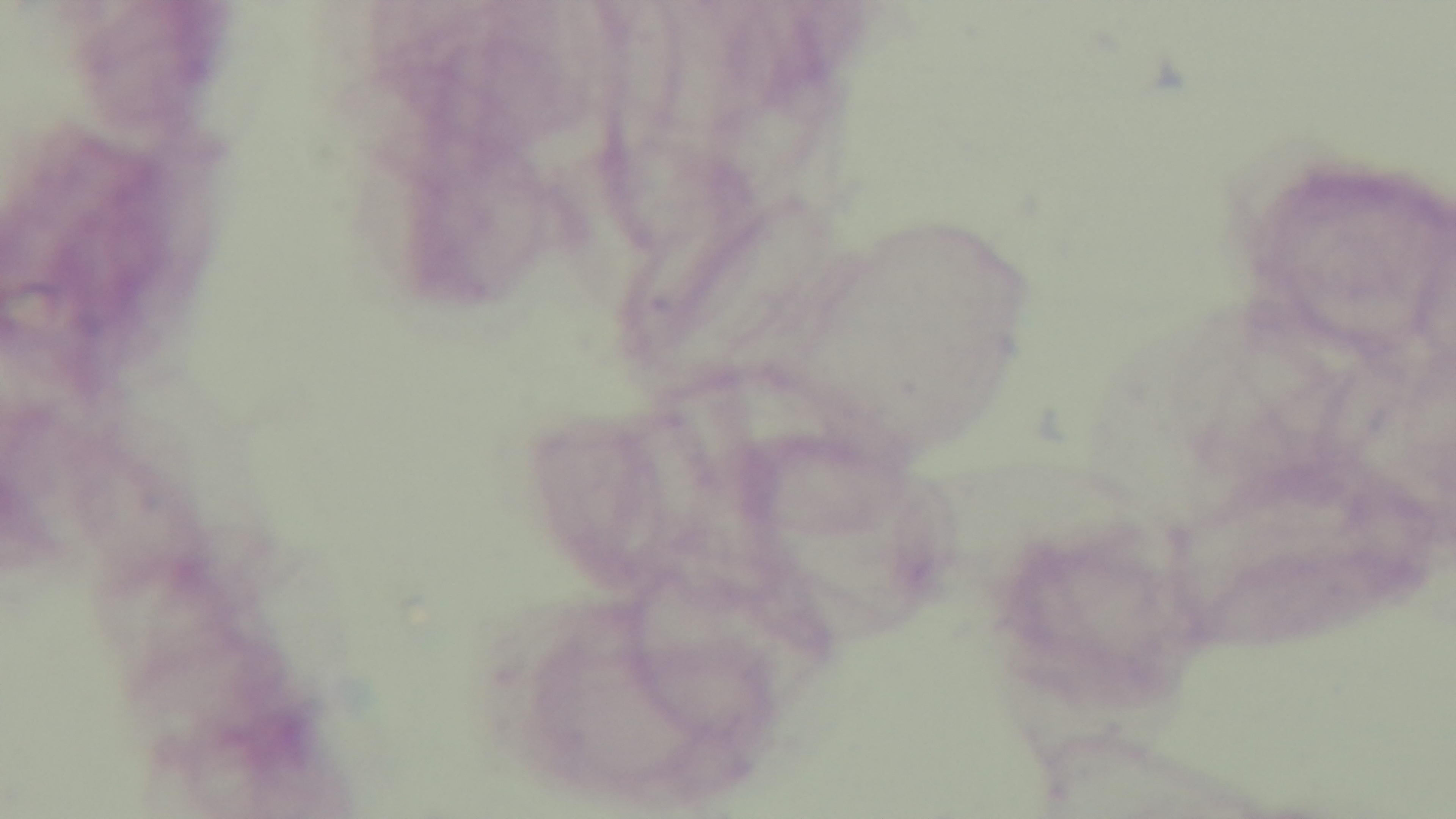

Summary:
  - Objective: 100x oil immersion
  - Malaria status: negative
  - Preparation: thick blood film
  - Modality: light microscopy
  - Field of view: single
  - Stain: Giemsa
  - Capture: mounted 4K digital camera